Assess the morphology of the red blood cells.
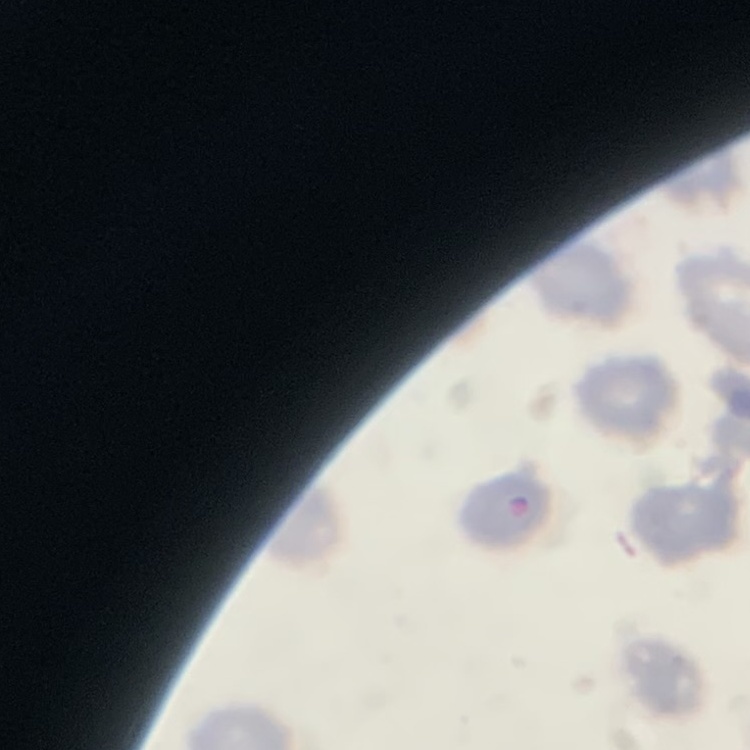

No rouleaux formation.

Summary:
  - Stain: Field's or Giemsa
  - Image type: one tile cut from a larger photomicrograph
  - Preparation: thin blood smear